Give the position of every Plasmodium parasite visible.
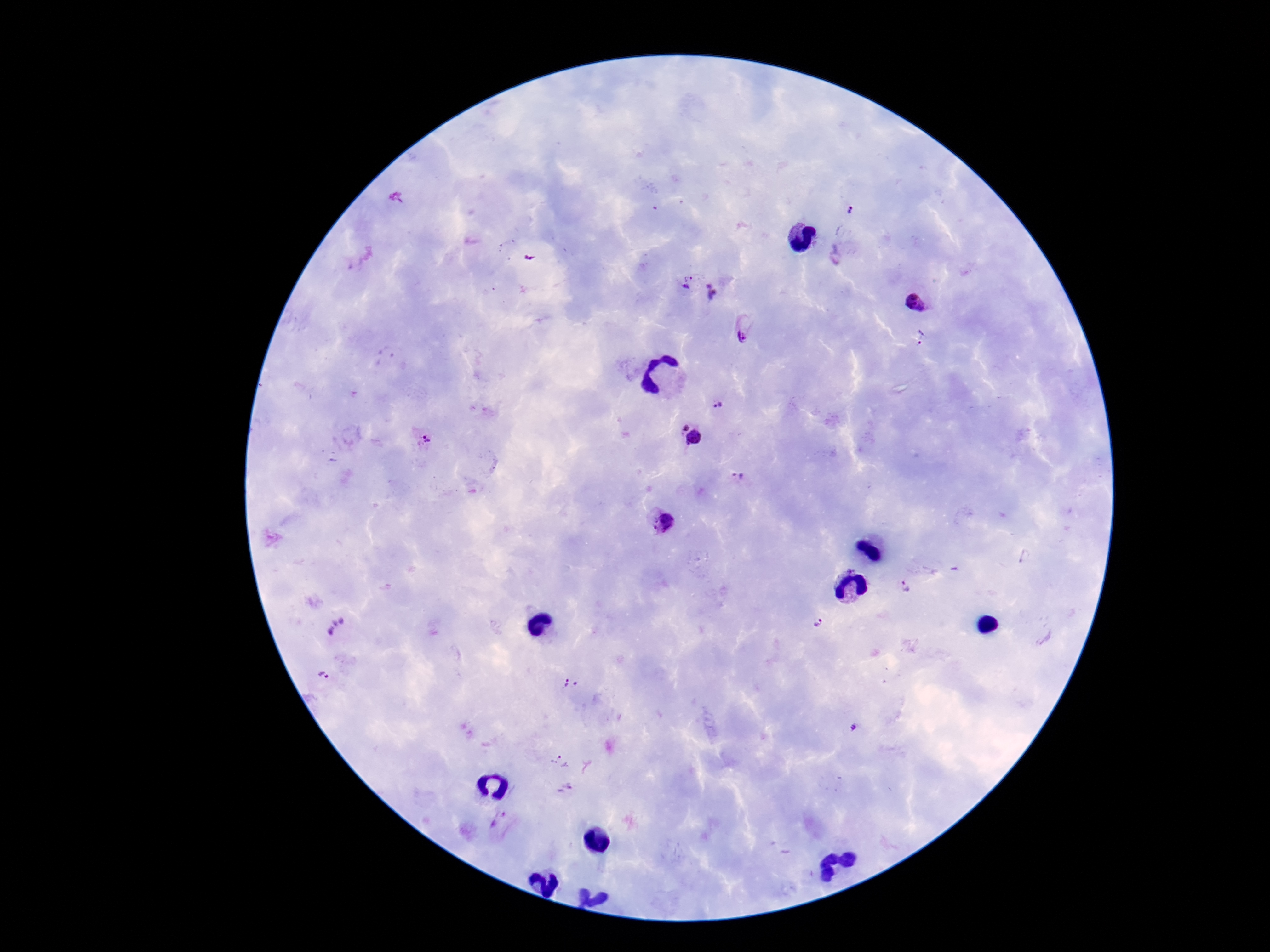
Approximate centers as {x, y} in pixels.
Plasmodium parasites: {849, 214}, {836, 256}, {685, 284}, {716, 293}, {916, 303}, {744, 330}, {923, 338}, {717, 405}, {683, 426}, {695, 438}, {425, 440}, {739, 479}, {665, 525}, {904, 588}, {818, 624}, {338, 626}, {325, 675}, {570, 684}, {853, 730}, {560, 762}, {565, 790}, {501, 819}.

Summary:
  - Magnification: 100x
  - Field of view: one from this slide
  - Stain: Giemsa
  - Preparation: thick blood smear
  - Image size: 1270×952 pixels
  - Patient malaria status: positive
  - Capture: smartphone camera through the microscope eyepiece